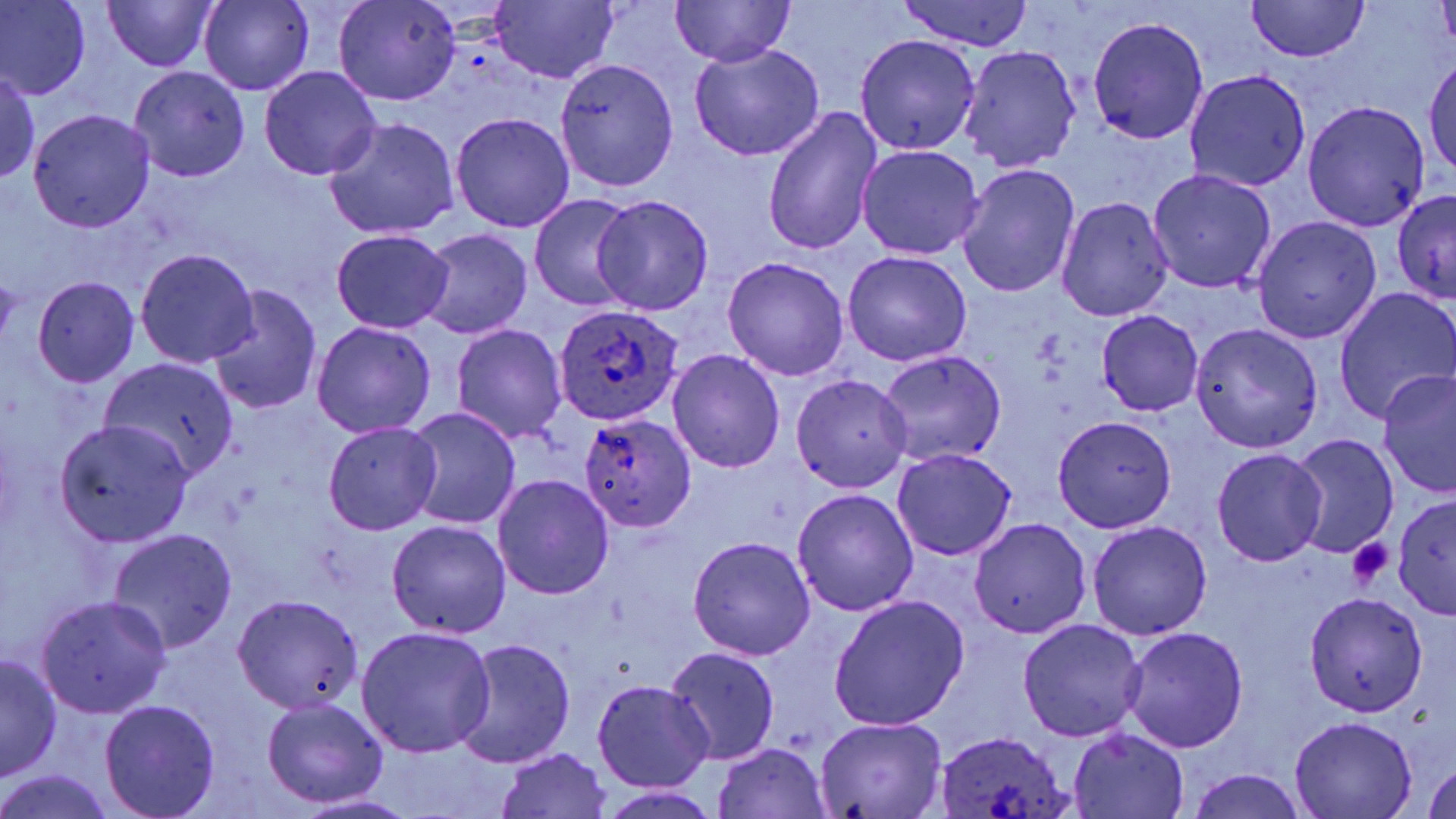
Summary:
  - Coordinate format: approximate bounding boxes as (x1,y1)-(x2,y2) corner pairs in pixels
  - Uninfected red blood cell locations: (102,0)-(218,71), (333,0)-(459,105), (1,1)-(90,100), (198,1)-(314,95), (487,1)-(618,85), (669,1)-(795,68), (893,1)-(1037,50), (1248,1)-(1370,62), (1087,16)-(1209,146), (853,34)-(980,155), (689,43)-(825,162), (958,45)-(1082,172), (1425,50)-(1456,180), (554,57)-(679,192), (129,67)-(250,182), (259,67)-(383,182), (1184,68)-(1311,192), (0,69)-(41,183), (1303,100)-(1431,231), (762,107)-(882,257), (28,109)-(154,232), (451,112)-(575,233), (324,118)-(459,240), (855,144)-(986,259), (958,165)-(1080,297), (1146,169)-(1277,294), (1391,190)-(1456,305), (531,195)-(641,308), (590,195)-(714,316), (1056,196)-(1175,322), (1253,216)-(1381,344), (331,229)-(454,333), (415,229)-(533,340), (134,248)-(260,367), (842,251)-(970,366), (722,256)-(850,381), (32,276)-(140,388), (209,284)-(321,416), (1335,288)-(1456,423), (1097,310)-(1204,416), (310,322)-(437,438), (1192,322)-(1324,454), (451,324)-(568,443), (668,349)-(786,472), (875,351)-(1007,467), (102,358)-(239,479), (1378,371)-(1456,498), (789,374)-(912,492), (404,407)-(523,530), (1053,415)-(1176,532), (54,419)-(194,545), (323,421)-(441,534), (1287,434)-(1398,558), (891,449)-(1017,561), (1211,449)-(1328,566), (492,475)-(614,601), (792,489)-(918,616), (1391,492)-(1455,617), (967,519)-(1091,640), (384,520)-(512,640), (1087,521)-(1212,640), (109,529)-(237,653), (687,535)-(816,660), (1304,592)-(1428,715), (829,594)-(970,730), (35,595)-(171,718), (232,596)-(363,713), (1019,618)-(1148,740), (355,625)-(496,759), (1120,627)-(1249,752), (452,638)-(575,770), (664,646)-(779,764), (1,654)-(61,783), (591,681)-(715,790), (261,697)-(389,808), (100,700)-(221,818), (813,716)-(948,818), (1288,717)-(1419,818), (1069,732)-(1187,819), (711,743)-(831,819), (494,748)-(613,819), (1424,760)-(1456,819), (1186,768)-(1309,819), (1,770)-(118,819), (596,787)-(725,816), (295,794)-(422,819)
  - Platelet locations: (1346,536)-(1394,589)
  - Plasmodium ovale-infected red blood cell locations: (553,303)-(685,425), (578,413)-(696,531), (933,730)-(1074,816)
  - Slide-level diagnosis: Plasmodium ovale
  - Preparation: thin blood smear
  - Magnification: 1000x
  - Image size: 1456×819 pixels
  - Stain: May-Grünwald-Giemsa
  - Field of view: single
  - Modality: light microscopy